State which parasite is depicted.
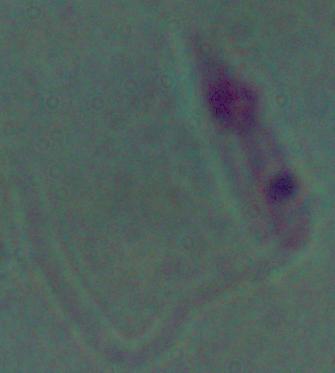
Leishmania.

Summary:
  - Modality: photomicrograph
  - Magnification: 1000x